Report the malaria status of this cell.
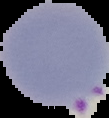
It is parasitized.

Image is 109×118 pixels. Segmented cell region on a black background. From a thin blood smear.